Identify the cell.
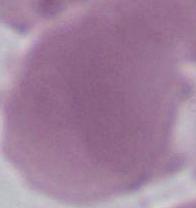
This is an erythrocyte.

Micrograph. 1000x magnification.